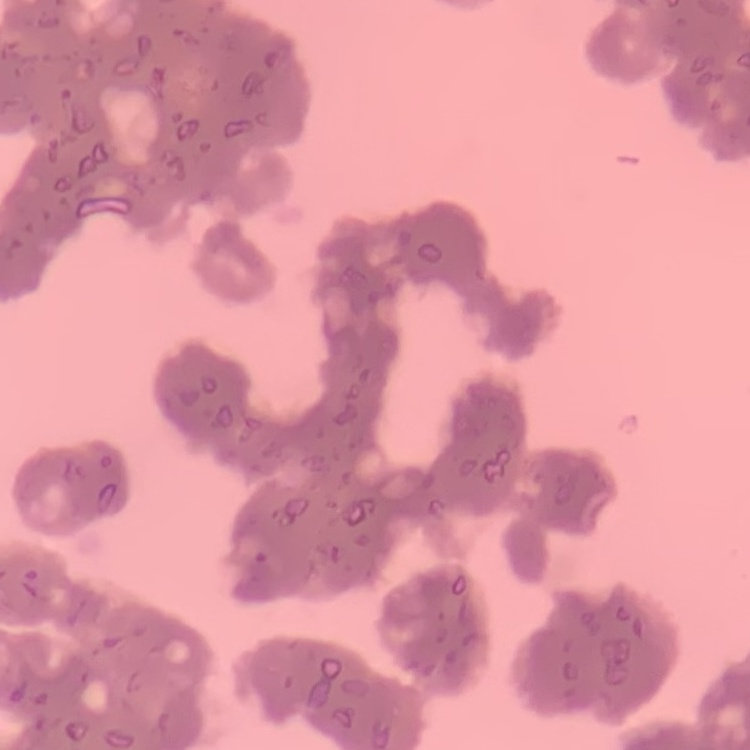
The erythrocytes show rouleaux formation. Field's or Giemsa stain. Square crop of a larger photomicrograph. Thin blood film.